Identify the blood parasite species.
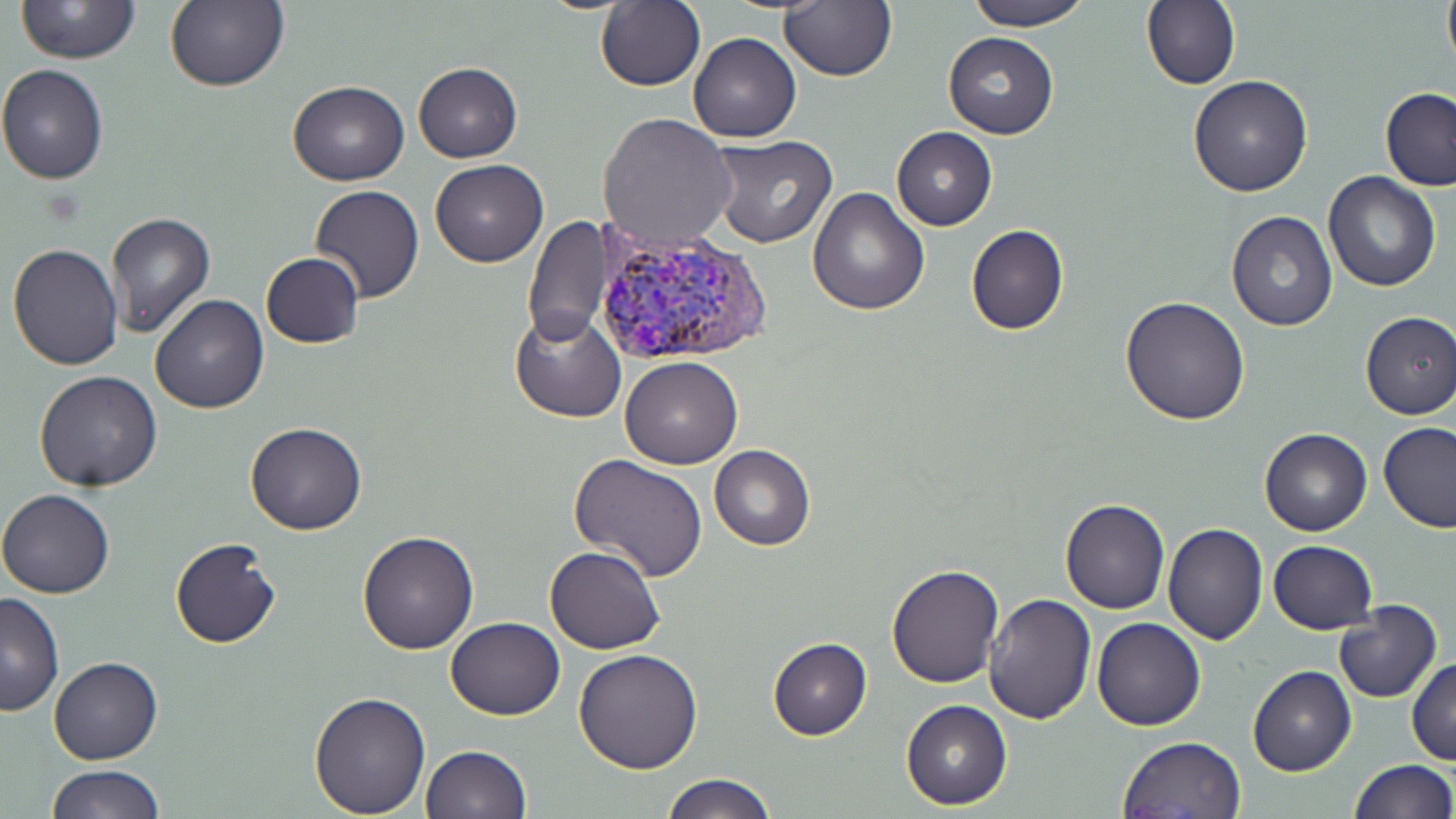
Plasmodium vivax.

Approximate bounding boxes as (x1, y1, x2, y2) in pixels. Plasmodium vivax-infected red blood cell locations: (593, 229, 774, 368). Uninfected red blood cell locations: (14, 0, 142, 64), (595, 0, 705, 91), (962, 0, 1096, 31), (1141, 0, 1241, 90), (1442, 0, 1456, 72), (166, 1, 289, 93), (778, 1, 896, 82), (688, 31, 802, 142), (943, 31, 1058, 140), (413, 62, 523, 162), (0, 64, 110, 183), (1187, 74, 1313, 197), (287, 79, 408, 185), (1379, 87, 1456, 192), (597, 110, 737, 249), (892, 127, 996, 230), (707, 134, 837, 248), (430, 159, 548, 267), (1322, 170, 1441, 292), (310, 185, 424, 304), (807, 185, 930, 315), (1225, 210, 1338, 331), (106, 211, 215, 338), (523, 216, 610, 349), (966, 223, 1068, 335), (7, 244, 124, 370), (260, 252, 364, 347), (150, 294, 270, 413), (1121, 294, 1251, 426), (510, 307, 627, 422), (1358, 311, 1456, 420), (621, 356, 743, 469), (35, 371, 164, 492), (244, 421, 367, 535), (1378, 422, 1455, 532), (1259, 426, 1372, 537), (710, 444, 814, 549), (569, 454, 708, 582), (0, 489, 117, 598), (1060, 499, 1169, 614), (1162, 523, 1267, 645), (358, 530, 478, 654), (169, 537, 281, 648), (1268, 540, 1378, 634), (545, 546, 666, 654), (884, 564, 1004, 686), (0, 593, 63, 717), (985, 593, 1097, 725), (1333, 601, 1442, 704), (445, 616, 565, 720), (1092, 617, 1206, 731), (767, 637, 872, 741), (574, 647, 704, 773), (49, 656, 161, 765), (1407, 658, 1456, 765), (1248, 666, 1356, 777), (309, 690, 430, 817), (900, 699, 1012, 810), (1117, 735, 1246, 817), (420, 744, 531, 818), (1347, 758, 1454, 818), (43, 763, 164, 818), (662, 774, 780, 819). Optical microscopy. Single field of view. Image is 1456×819 pixels. May-Grünwald-Giemsa stain. Thin blood film. 1000x magnification.